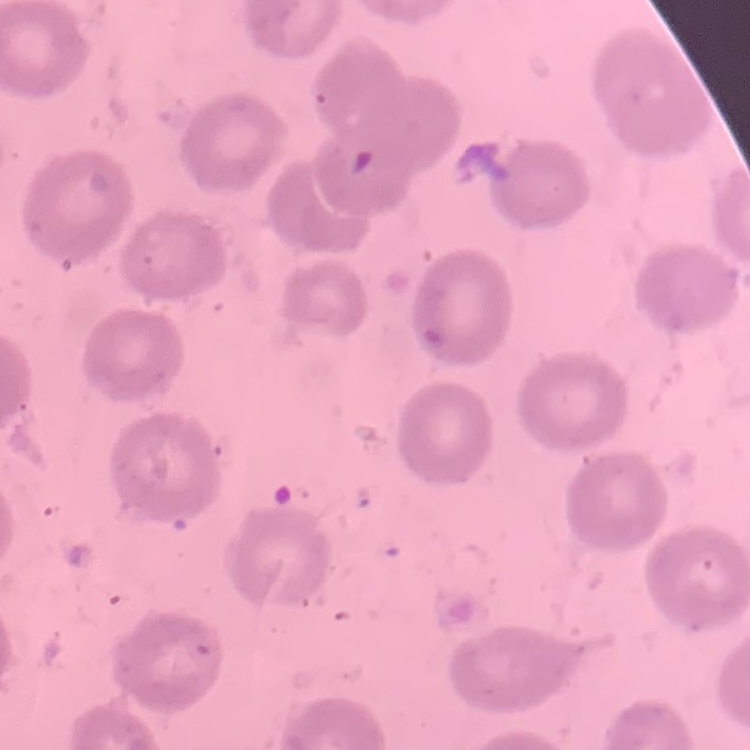

erythrocyte morphology = no rouleaux formation
stain = Field's or Giemsa
image type = one tile cut from a larger photomicrograph
preparation = thin blood film